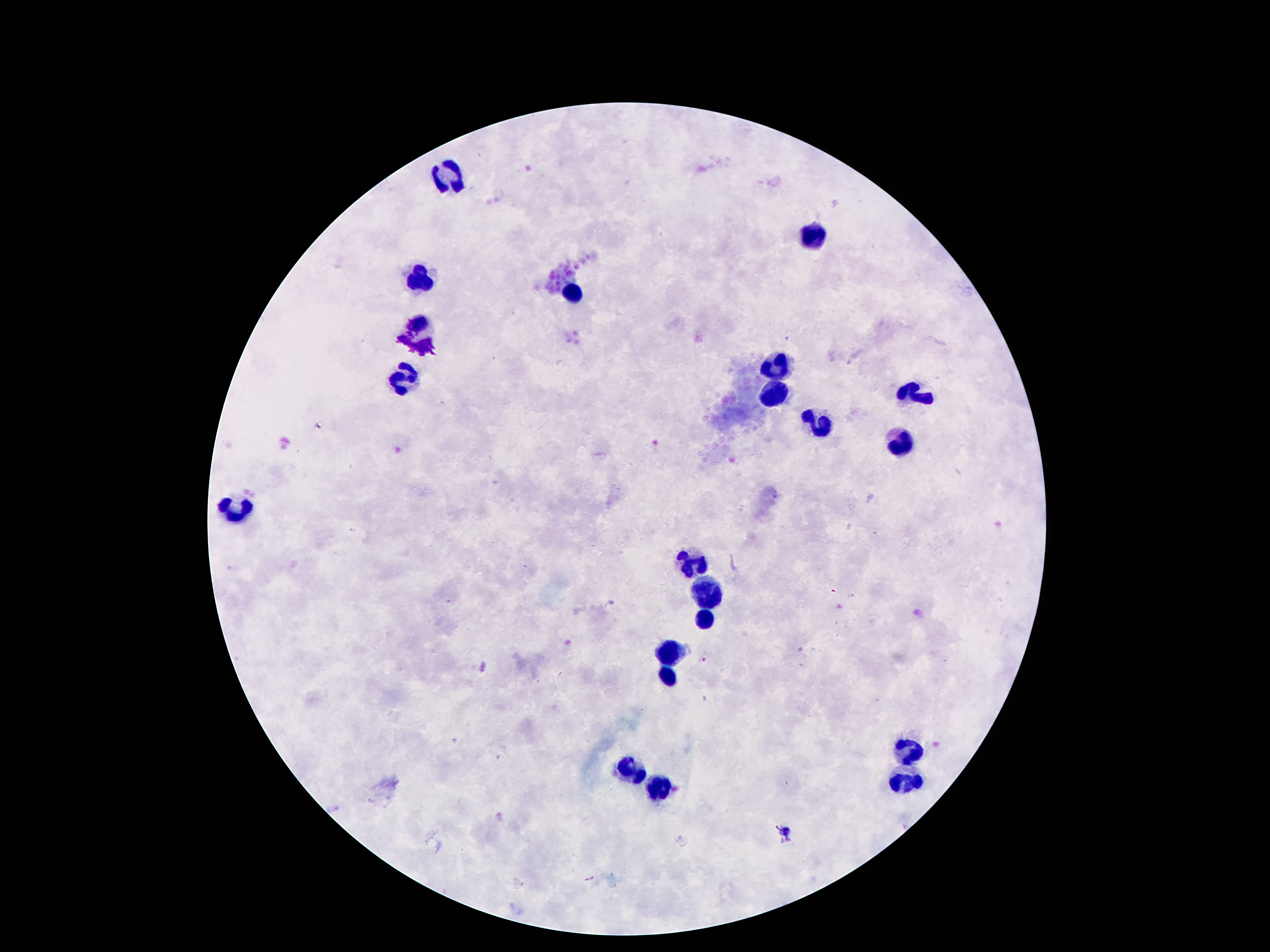

Approximate centers as {x, y} in pixels.
Summary:
  - Leukocyte locations: {447, 178}, {818, 236}, {419, 279}, {570, 295}, {417, 336}, {775, 361}, {404, 377}, {910, 390}, {773, 392}, {820, 425}, {902, 445}, {238, 509}, {693, 564}, {708, 592}, {705, 623}, {671, 654}, {664, 674}, {912, 755}, {628, 772}, {908, 786}, {658, 788}
  - Preparation: thick blood smear
  - Magnification: 100x
  - Field of view: one from this slide
  - Capture: smartphone camera through the microscope eyepiece
  - Stain: Giemsa
  - Image size: 1270×952 pixels
  - Patient malaria status: uninfected